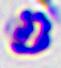

A leukocyte is seen. Micrograph. Captured at 400x magnification.